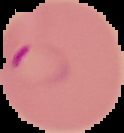

Image is 124×133 pixels. From a thin blood film. The area outside the segmented cell region is set to black. Malaria status: parasitized.